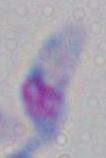
Micrograph. 1000x magnification. Toxoplasma gondii is seen.